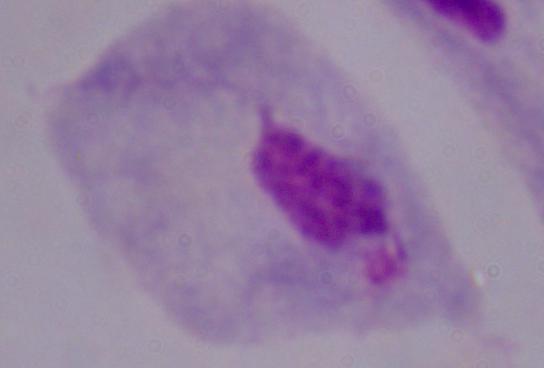 Micrograph. 1000x magnification. A trichomonad is seen.